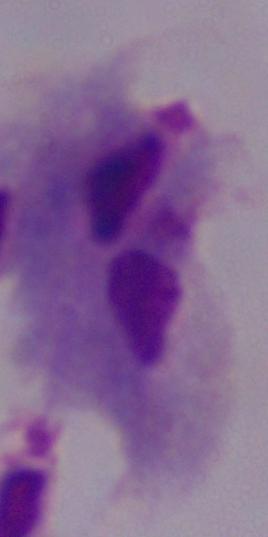
{
  "magnification": "1000x",
  "identification": "trichomonad",
  "modality": "micrograph"
}